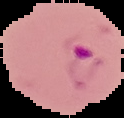
Malaria status: parasitized. From a thin blood smear. Image is 124×118 pixels. Cell region segmented out of the field of view; the surrounding area is masked to black.